Report the malaria status of this cell.
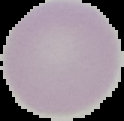

It is uninfected.

{
  "image_size": "124×121 pixels",
  "image_type": "cell region segmented out of the field of view; surrounding area masked to black",
  "preparation": "thin blood smear"
}